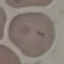
Result: no malaria parasites detected. Giemsa-stained preparation. Photographed with a smartphone camera at the microscope eyepiece. Automatically extracted cell patch, resized to 64 × 64 pixels. Thin blood smear.